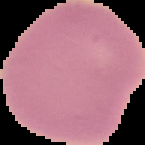 Malaria status: uninfected. Image is 145×145 pixels. Segmented cell region on a black background. From a thin blood smear.